State which parasite is depicted.
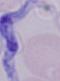

This is a trypanosome.

magnification = 1000x
modality = micrograph